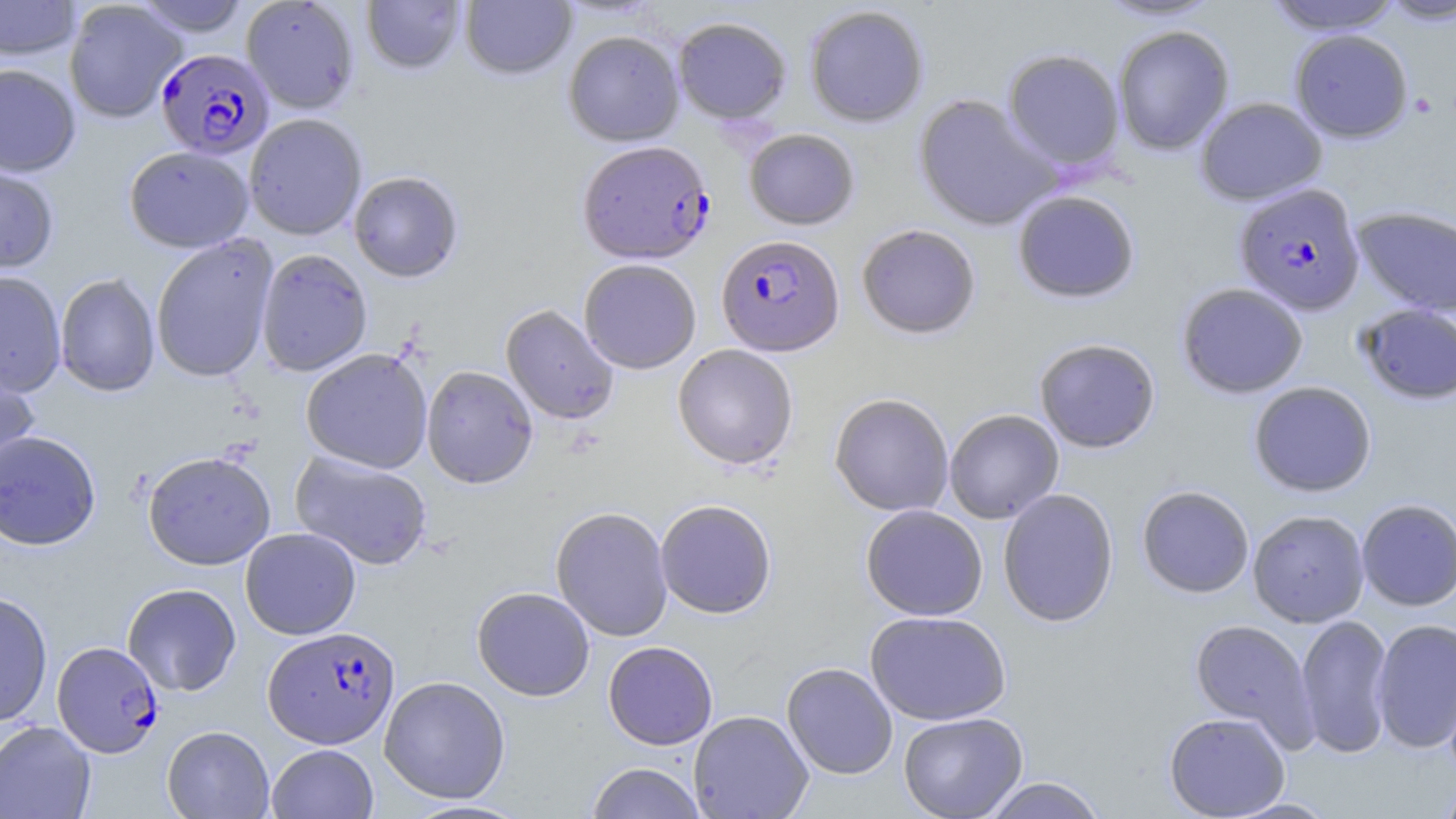

slide-level diagnosis = Plasmodium falciparum
preparation = thin blood smear
image size = 1456×819 pixels
uninfected red blood cell locations = approximate bounding boxes as [x1, y1, x2, y2] in pixels: [0, 0, 82, 61], [132, 0, 252, 38], [241, 0, 360, 115], [361, 0, 467, 76], [460, 0, 576, 81], [1093, 0, 1225, 23], [1263, 0, 1404, 35], [1376, 0, 1456, 27], [63, 1, 187, 123], [804, 5, 929, 128], [673, 17, 791, 125], [1113, 26, 1234, 155], [1290, 29, 1413, 142], [563, 30, 685, 146], [1003, 49, 1125, 172], [0, 64, 81, 177], [913, 94, 1060, 232], [1195, 97, 1327, 205], [244, 114, 367, 241], [744, 129, 859, 230], [124, 146, 254, 253], [0, 163, 59, 277], [348, 172, 464, 284], [1012, 190, 1139, 304], [1351, 206, 1456, 317], [856, 224, 981, 340], [150, 236, 279, 383], [256, 249, 373, 377], [579, 259, 701, 374], [0, 271, 67, 397], [55, 273, 161, 397], [1176, 282, 1308, 399], [1356, 304, 1456, 404], [500, 305, 618, 425], [1034, 338, 1161, 453], [672, 345, 798, 471], [300, 349, 433, 474], [0, 356, 40, 487], [421, 366, 538, 489], [1249, 381, 1377, 497], [829, 394, 954, 517], [944, 409, 1064, 523], [0, 430, 101, 552], [290, 451, 432, 571], [142, 452, 276, 571], [1137, 485, 1254, 598], [997, 488, 1119, 628], [1356, 499, 1456, 611], [655, 500, 777, 619], [861, 505, 988, 621], [551, 507, 673, 642], [1247, 510, 1369, 627], [240, 528, 361, 640], [122, 584, 241, 697], [472, 586, 595, 701], [0, 591, 53, 727], [865, 611, 1012, 725], [1295, 614, 1394, 758], [1190, 618, 1317, 745], [1371, 618, 1456, 754], [603, 641, 718, 750], [782, 662, 898, 780], [379, 675, 510, 804], [688, 710, 813, 818], [898, 711, 1028, 819], [1163, 712, 1290, 818], [0, 720, 96, 819], [162, 726, 275, 818], [267, 743, 378, 818], [585, 762, 707, 819], [981, 776, 1108, 818], [1436, 778, 1456, 819], [1222, 797, 1340, 818], [401, 799, 532, 818]
field of view = one of a larger specimen
stain = May-Grünwald-Giemsa
magnification = 1000x
Plasmodium falciparum-infected red blood cell locations = approximate bounding boxes as [x1, y1, x2, y2] in pixels: [155, 49, 274, 160], [577, 141, 715, 265], [1234, 183, 1365, 316], [716, 234, 845, 356], [263, 626, 400, 748], [52, 641, 164, 758]
modality = optical microscopy
platelet locations = approximate bounding boxes as [x1, y1, x2, y2] in pixels: [1410, 91, 1439, 118]